Describe the morphology of the red blood cells.
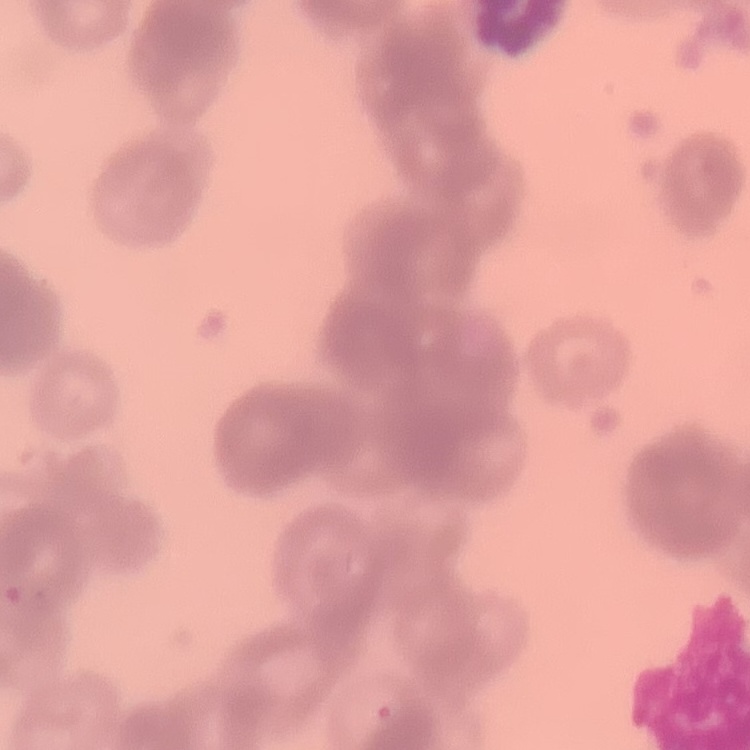
Rouleaux formation.

Summary:
  - Preparation: thin blood film
  - Stain: Field's or Giemsa
  - Image type: one tile cut from a larger photomicrograph